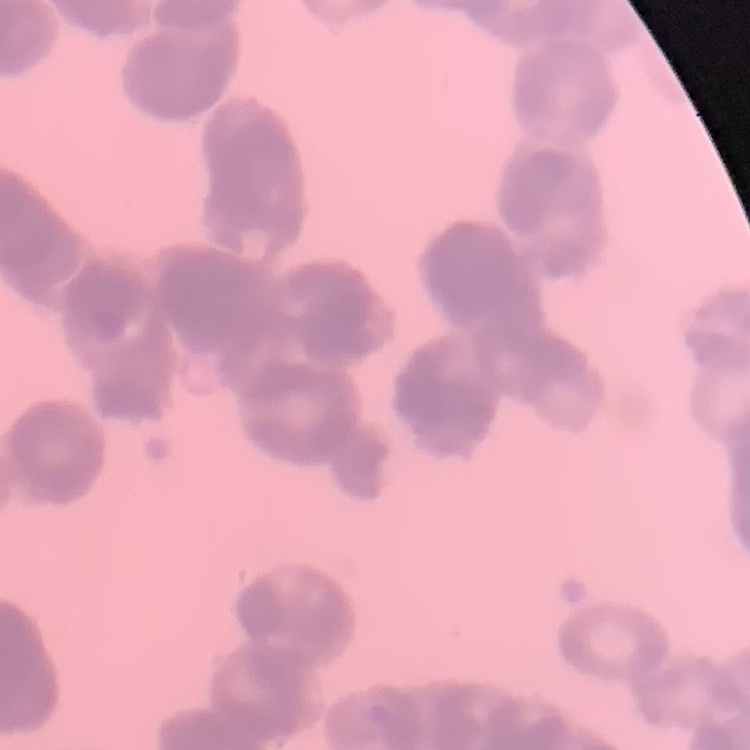

The erythrocytes show rouleaux formation. One tile cut from a larger photomicrograph. Thin blood smear. Field's or Giemsa stain.